Classify this cell by malaria status.
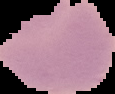
Uninfected.

The area outside the segmented cell region is set to black. From a thin blood smear. Image is 115×94 pixels.